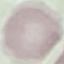
result = negative for malaria parasites
capture = smartphone through the microscope eyepiece
preparation = thin blood film
stain = Giemsa
image type = automatically extracted cell patch, resized to 64 × 64 pixels